Give the position of every Plasmodium parasite and every leukocyte.
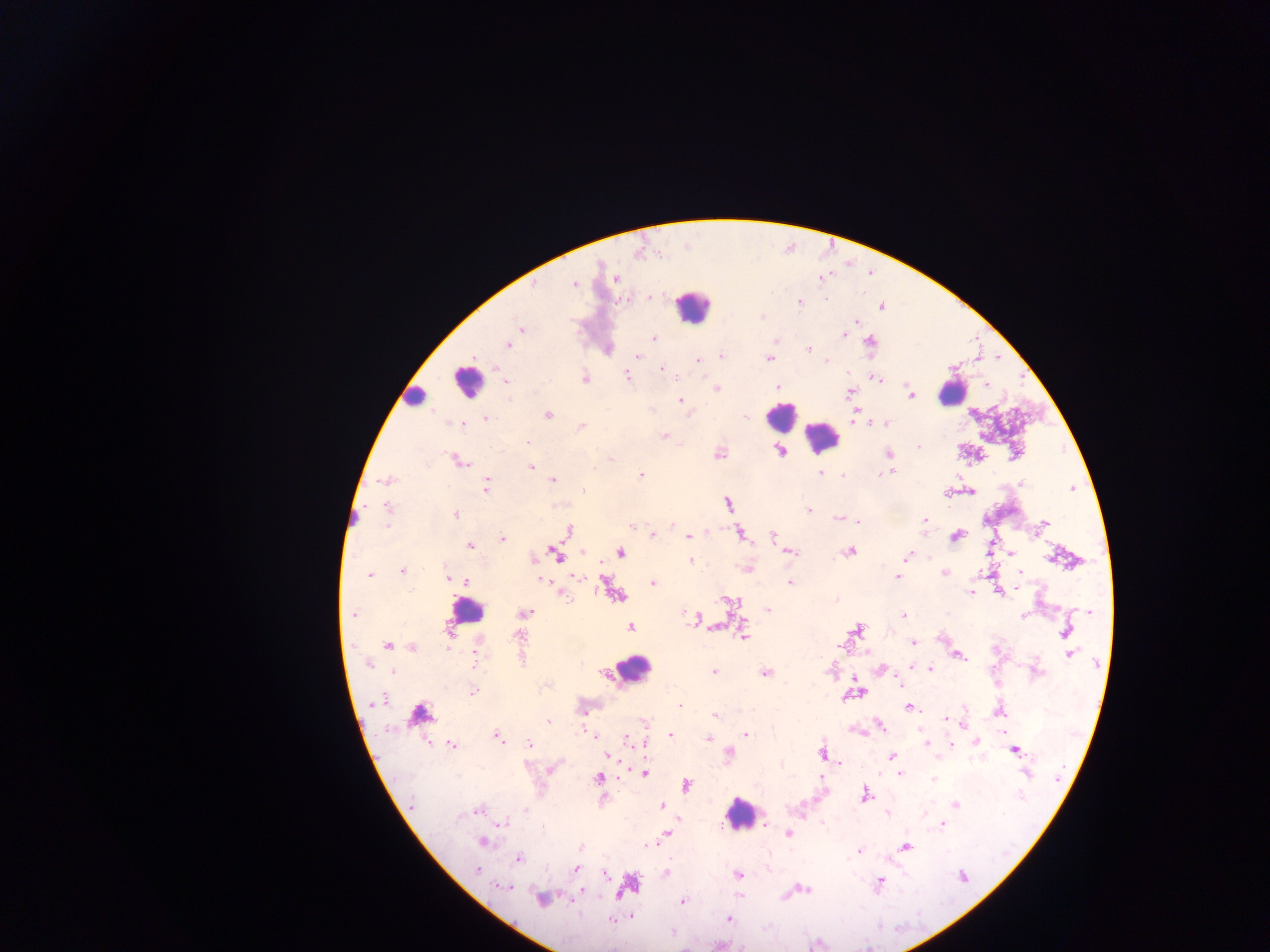

Approximate centers as {x, y} in pixels.
Plasmodium parasites: {616, 279}, {573, 283}, {799, 301}, {882, 306}, {520, 328}, {843, 334}, {654, 337}, {774, 339}, {870, 343}, {508, 345}, {606, 349}, {808, 349}, {721, 355}, {638, 356}, {769, 358}, {698, 360}, {827, 360}, {661, 368}, {626, 375}, {876, 377}, {584, 379}, {505, 383}, {986, 384}, {777, 387}, {716, 388}, {850, 392}, {911, 395}, {680, 400}, {853, 414}, {547, 415}, {486, 418}, {883, 422}, {463, 423}, {581, 426}, {664, 436}, {526, 441}, {780, 451}, {719, 453}, {888, 453}, {610, 458}, {457, 460}, {531, 466}, {820, 471}, {892, 471}, {641, 475}, {844, 475}, {552, 479}, {385, 480}, {485, 485}, {583, 490}, {970, 490}, {947, 493}, {727, 502}, {388, 508}, {809, 510}, {455, 514}, {838, 518}, {856, 520}, {923, 520}, {1043, 525}, {632, 526}, {567, 530}, {740, 533}, {652, 535}, {956, 535}, {688, 536}, {773, 536}, {502, 538}, {470, 545}, {989, 548}, {848, 551}, {582, 552}, {620, 552}, {788, 552}, {1012, 552}, {557, 555}, {907, 555}, {533, 558}, {691, 560}, {747, 568}, {402, 570}, {1019, 571}, {945, 573}, {368, 574}, {578, 576}, {897, 576}, {448, 577}, {539, 578}, {465, 581}, {789, 582}, {653, 583}, {610, 589}, {998, 590}, {560, 592}, {970, 592}, {616, 595}, {728, 600}, {767, 609}, {1089, 612}, {353, 613}, {524, 613}, {902, 616}, {695, 620}, {631, 626}, {856, 629}, {447, 631}, {1066, 632}, {742, 634}, {942, 637}, {913, 642}, {388, 644}, {412, 647}, {838, 647}, {1070, 654}, {957, 655}, {474, 657}, {368, 663}, {910, 666}, {931, 668}, {393, 670}, {880, 670}, {714, 671}, {765, 672}, {855, 679}, {898, 682}, {472, 692}, {856, 692}, {862, 693}, {850, 695}, {377, 701}, {680, 705}, {907, 707}, {582, 710}, {999, 710}, {419, 715}, {715, 715}, {946, 719}, {548, 721}, {645, 722}, {963, 723}, {878, 724}, {859, 730}, {745, 733}, {594, 735}, {670, 735}, {498, 737}, {626, 739}, {708, 739}, {976, 741}, {712, 742}, {925, 742}, {645, 743}, {950, 743}, {452, 745}, {530, 745}, {1014, 750}, {728, 752}, {822, 753}, {608, 756}, {892, 757}, {839, 763}, {551, 768}, {643, 773}, {900, 773}, {598, 778}, {933, 780}, {686, 784}, {865, 794}, {955, 804}, {411, 805}, {661, 805}, {477, 810}, {887, 812}, {503, 822}, {941, 822}, {764, 824}, {788, 833}, {663, 835}, {481, 842}, {905, 846}, {581, 847}, {859, 850}, {518, 858}, {575, 868}, {476, 870}, {665, 873}, {605, 874}, {738, 874}, {879, 883}, {627, 885}, {503, 886}, {806, 889}, {583, 893}, {540, 899}, {682, 901}, {630, 916}, {727, 918}, {610, 920}, {671, 932}.
Leukocytes: {692, 308}, {468, 381}, {952, 392}, {413, 398}, {780, 417}, {820, 437}, {466, 612}, {631, 668}, {740, 814}.

Summary:
  - Image size: 1270×952 pixels
  - Preparation: thick blood film
  - Capture: mobile-phone photograph through a microscope
  - Field of view: single
  - Country: Ghana